Classify this cell by malaria status.
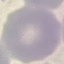

It is uninfected.

capture = smartphone camera at the microscope eyepiece
image type = automatically extracted cell patch, resized to 64 × 64 pixels
preparation = thin smear
stain = Giemsa